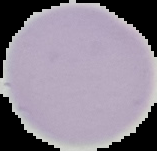
image size = 157×151 pixels
result = negative for malaria parasites
image type = segmented cell region with the area outside set to black
preparation = thin blood film